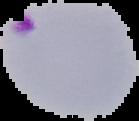

image type = segmented cell region with the area outside set to black
image size = 139×121 pixels
preparation = thin blood film
malaria status = parasitized